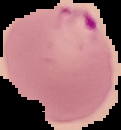
The area outside the segmented cell region is set to black. Image is 121×130 pixels. From a thin blood film. Malaria status: parasitized.